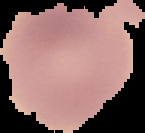
{
  "preparation": "thin blood film",
  "result": "no malaria parasites seen",
  "image_type": "cell region segmented out of the field of view; surrounding area masked to black",
  "image_size": "145×133 pixels"
}